Give the extent of all Plasmodium malariae-infected red blood cells.
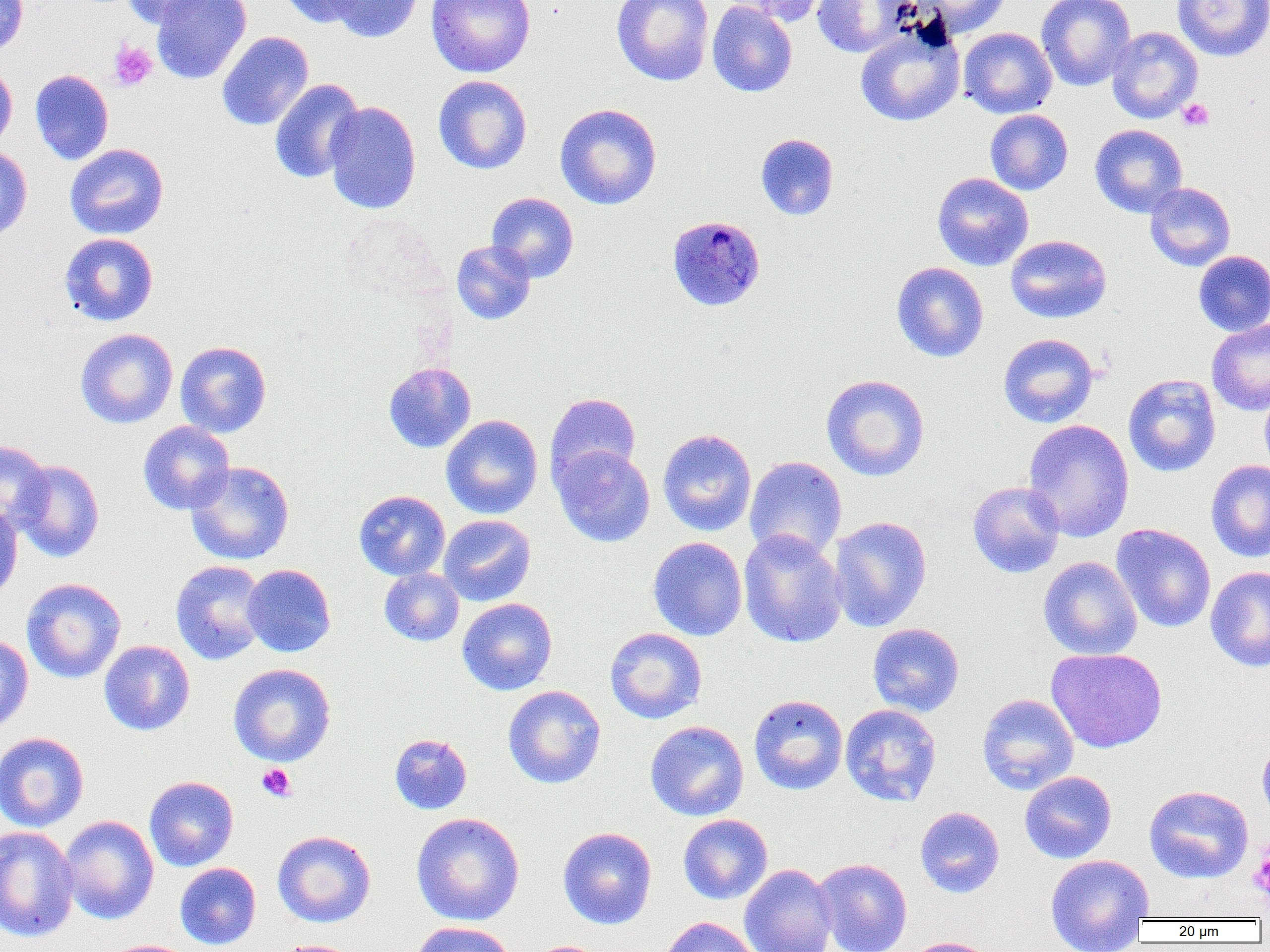
Approximate bounding boxes as (x1,y1)-(x2,y2) corner pairs in pixels.
Plasmodium malariae-infected red blood cells: (666,215)-(766,311).

slide-level diagnosis = Plasmodium malariae
platelet locations = approximate bounding boxes as (x1,y1)-(x2,y2) corner pairs in pixels: (108,41)-(158,91), (1177,99)-(1214,132), (256,763)-(297,802), (1249,847)-(1270,901)
uninfected red blood cell locations = approximate bounding boxes as (x1,y1)-(x2,y2) corner pairs in pixels: (0,0)-(29,56), (123,0)-(220,28), (151,0)-(252,84), (276,0)-(365,27), (326,0)-(424,43), (425,0)-(536,78), (612,0)-(714,86), (725,0)-(828,27), (812,0)-(908,58), (912,0)-(1013,38), (1036,0)-(1136,92), (1172,0)-(1270,61), (707,1)-(797,98), (855,21)-(965,127), (1107,26)-(1203,124), (959,27)-(1057,118), (217,31)-(314,131), (0,61)-(17,154), (30,69)-(114,165), (433,75)-(532,174), (269,79)-(365,184), (324,101)-(422,215), (555,103)-(662,210), (985,109)-(1073,195), (1089,124)-(1188,217), (755,133)-(839,220), (65,143)-(169,240), (0,145)-(32,240), (932,172)-(1034,271), (1145,182)-(1236,271), (486,192)-(579,283), (59,233)-(159,326), (1005,234)-(1112,324), (451,240)-(536,325), (1193,250)-(1270,336), (891,262)-(989,362), (1206,319)-(1270,416), (75,328)-(178,428), (998,333)-(1099,428), (175,341)-(272,438), (384,362)-(476,453), (1123,373)-(1221,477), (820,374)-(930,482), (1259,383)-(1270,478), (545,392)-(641,489), (441,414)-(543,519), (1022,418)-(1135,542), (138,421)-(235,514), (657,428)-(757,536), (0,440)-(52,529), (551,444)-(655,547), (744,455)-(847,561), (11,459)-(104,562), (1206,459)-(1270,562), (185,461)-(294,565), (967,481)-(1065,578), (354,490)-(450,580), (0,500)-(23,605), (438,514)-(536,607), (828,516)-(932,632), (1111,524)-(1216,633), (738,529)-(848,649), (647,537)-(747,641), (1038,556)-(1142,660), (171,560)-(268,665), (242,564)-(336,657), (1205,566)-(1270,672), (379,568)-(465,646), (22,577)-(126,683), (457,597)-(557,696), (867,623)-(965,717), (605,627)-(707,724), (0,635)-(34,733), (99,640)-(195,736), (1046,647)-(1167,753), (228,663)-(336,766), (503,685)-(606,789), (977,693)-(1079,795), (749,694)-(848,795), (840,703)-(942,806), (645,720)-(749,821), (0,732)-(89,832), (389,733)-(472,814), (1257,739)-(1270,829), (1019,771)-(1117,863), (144,776)-(239,871), (1144,785)-(1254,884), (915,806)-(1005,898), (411,811)-(525,926), (58,814)-(159,925), (678,814)-(772,904), (0,826)-(79,943), (558,827)-(657,929), (272,830)-(376,928), (1044,854)-(1154,951), (813,858)-(913,952), (175,862)-(261,950), (739,863)-(837,952), (657,916)-(761,952), (408,921)-(518,952), (901,936)-(997,952), (99,939)-(199,952), (272,939)-(367,952)
image size = 1270×952 pixels
preparation = thin blood film
modality = optical microscopy
field of view = single
magnification = 1000x